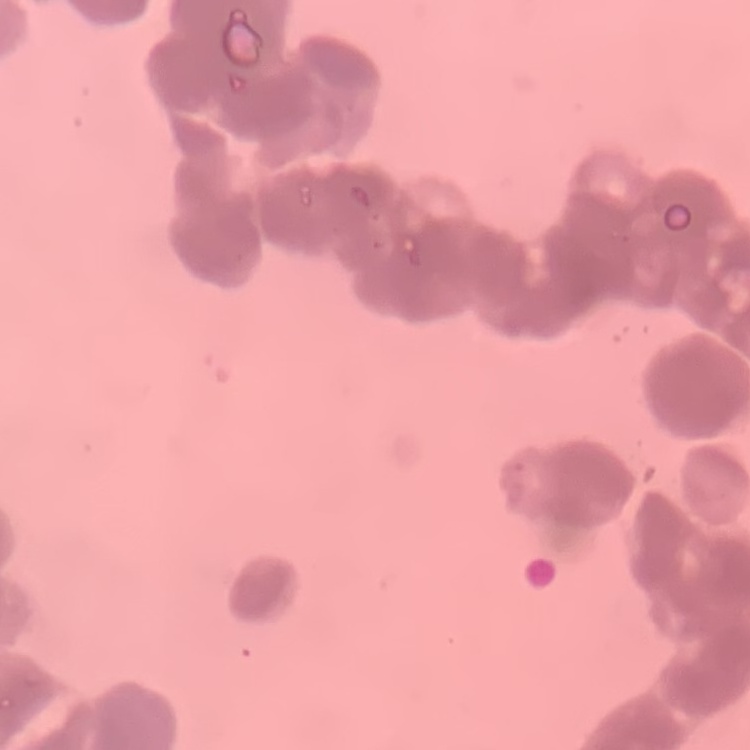 The red blood cells show rouleaux formation. Stained with either Field's or Giemsa. Square crop of a larger photomicrograph. Thin blood film.